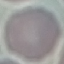

Summary:
  - Malaria status: uninfected
  - Image type: automatically extracted cell patch, resized to 64 × 64 pixels
  - Preparation: thin smear
  - Stain: Giemsa
  - Capture: smartphone through the microscope eyepiece